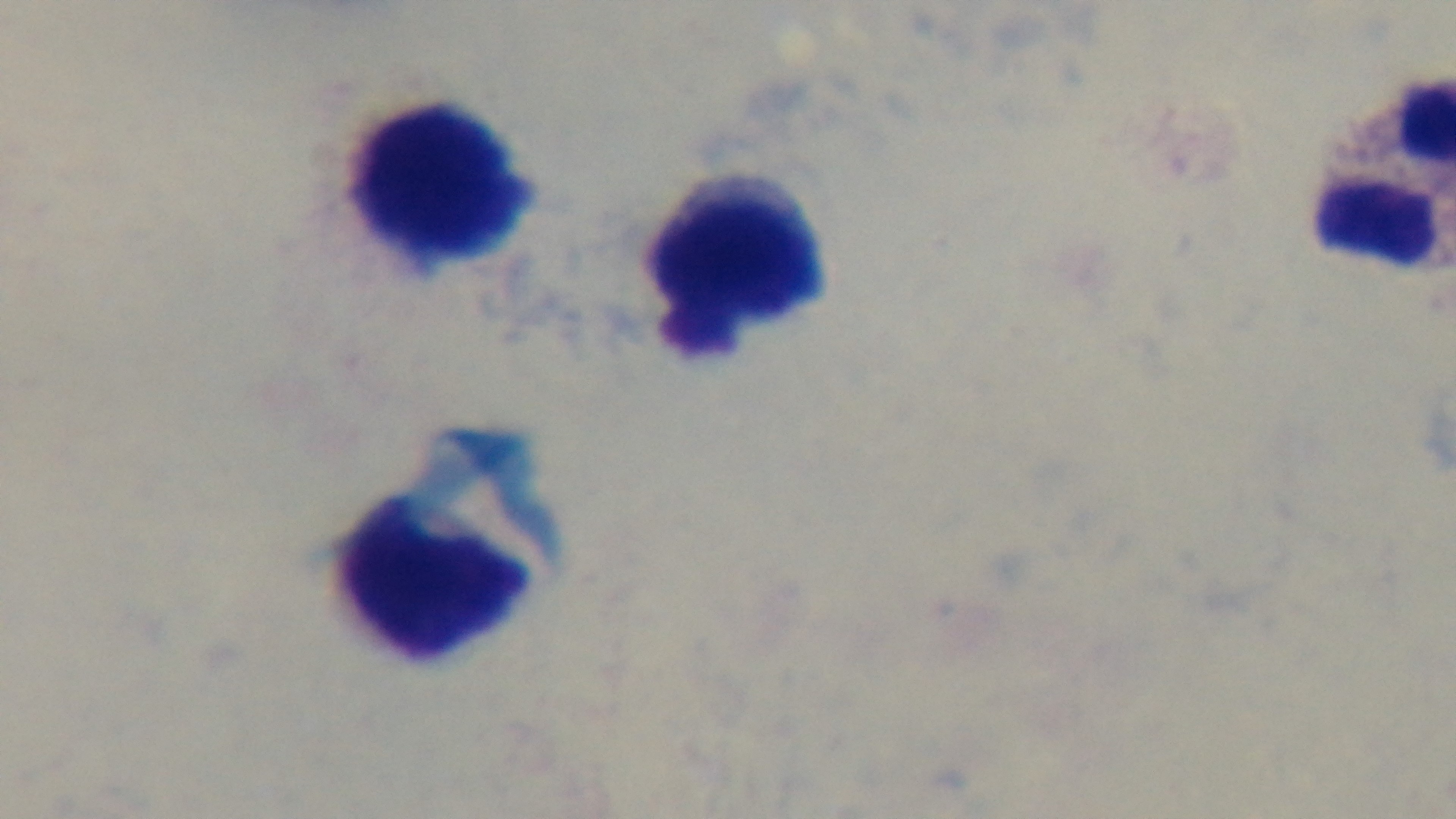
Summary:
  - Capture: mounted 4K digital camera
  - Preparation: thick smear
  - Malaria status: negative
  - Modality: light microscopy
  - Stain: Giemsa
  - Objective: 100x oil immersion
  - Field of view: one from the slide